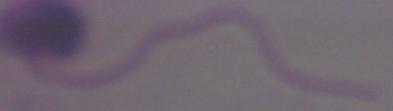 1000x magnification. Photomicrograph. A Leishmania parasite is shown.